Outline each Plasmodium vivax-infected red blood cell.
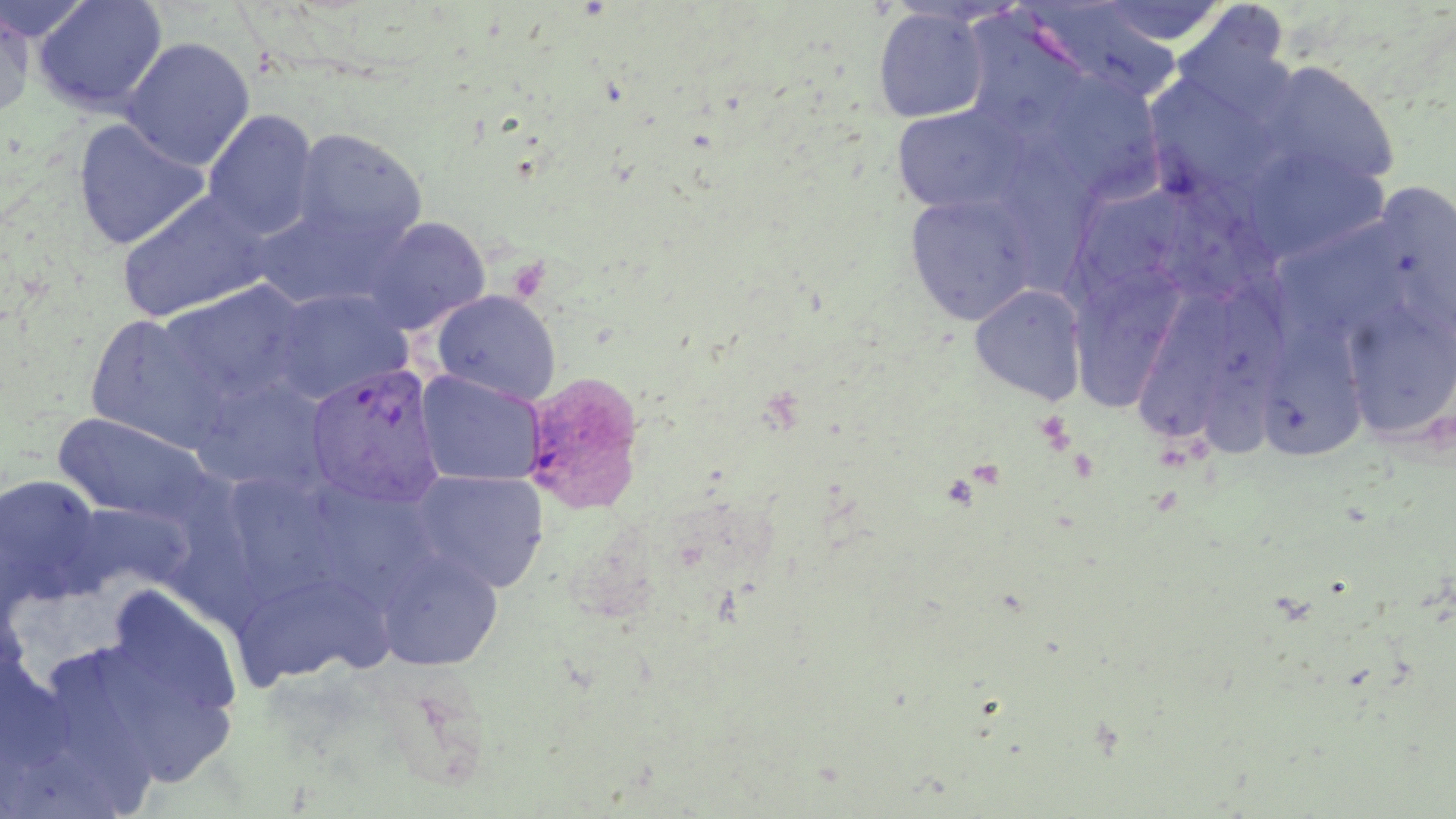

Approximate bounding boxes as [x1, y1, x2, y2] in pixels.
Plasmodium vivax-infected red blood cells: [305, 362, 445, 510], [522, 369, 647, 514].

slide-level diagnosis = Plasmodium vivax
image size = 1456×819 pixels
modality = optical microscopy
platelet locations = approximate bounding boxes as [x1, y1, x2, y2] in pixels: [1034, 410, 1075, 455]
magnification = 1000x
preparation = thin blood film
uninfected red blood cell locations = approximate bounding boxes as [x1, y1, x2, y2] in pixels: [0, 0, 95, 43], [33, 0, 167, 116], [1090, 1, 1233, 46], [1017, 2, 1184, 104], [0, 4, 33, 118], [1178, 4, 1291, 112], [872, 7, 991, 123], [120, 37, 255, 171], [1259, 60, 1401, 190], [1151, 75, 1276, 198], [1038, 76, 1164, 196], [891, 104, 1027, 216], [202, 110, 320, 240], [73, 118, 210, 250], [290, 128, 428, 254], [1009, 129, 1108, 293], [1242, 147, 1389, 263], [1374, 184, 1456, 343], [1061, 186, 1195, 313], [117, 190, 272, 324], [904, 191, 1039, 326], [249, 203, 400, 311], [362, 216, 490, 335], [1070, 262, 1184, 417], [160, 282, 309, 406], [969, 284, 1088, 406], [1135, 289, 1232, 448], [1200, 289, 1297, 467], [269, 290, 412, 405], [431, 290, 562, 405], [1340, 300, 1456, 441], [84, 313, 230, 454], [1266, 313, 1358, 470], [416, 371, 543, 486], [189, 378, 332, 496], [52, 411, 218, 530], [227, 466, 339, 606], [411, 470, 549, 593], [0, 473, 106, 606], [173, 481, 263, 636], [318, 485, 443, 607], [375, 549, 504, 671], [243, 577, 396, 690], [102, 584, 241, 733], [92, 642, 238, 788], [53, 654, 158, 815]
stain = May-Grünwald-Giemsa
field of view = one of a larger specimen